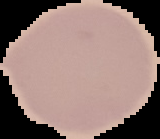
Summary:
  - Image size: 160×139 pixels
  - Result: no Plasmodium parasites detected
  - Preparation: thin blood smear
  - Image type: segmented cell region on a black background